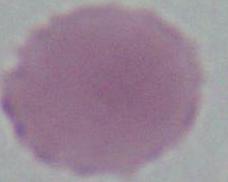

Summary:
  - Magnification: 1000x
  - Identification: erythrocyte
  - Modality: micrograph